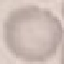 Malaria status: uninfected. Giemsa-stained preparation. Cell patch, automatically extracted from a larger field of view and resized to 64 × 64 pixels. Acquired by smartphone through the microscope eyepiece. Thin blood film.